Identify the preparation type.
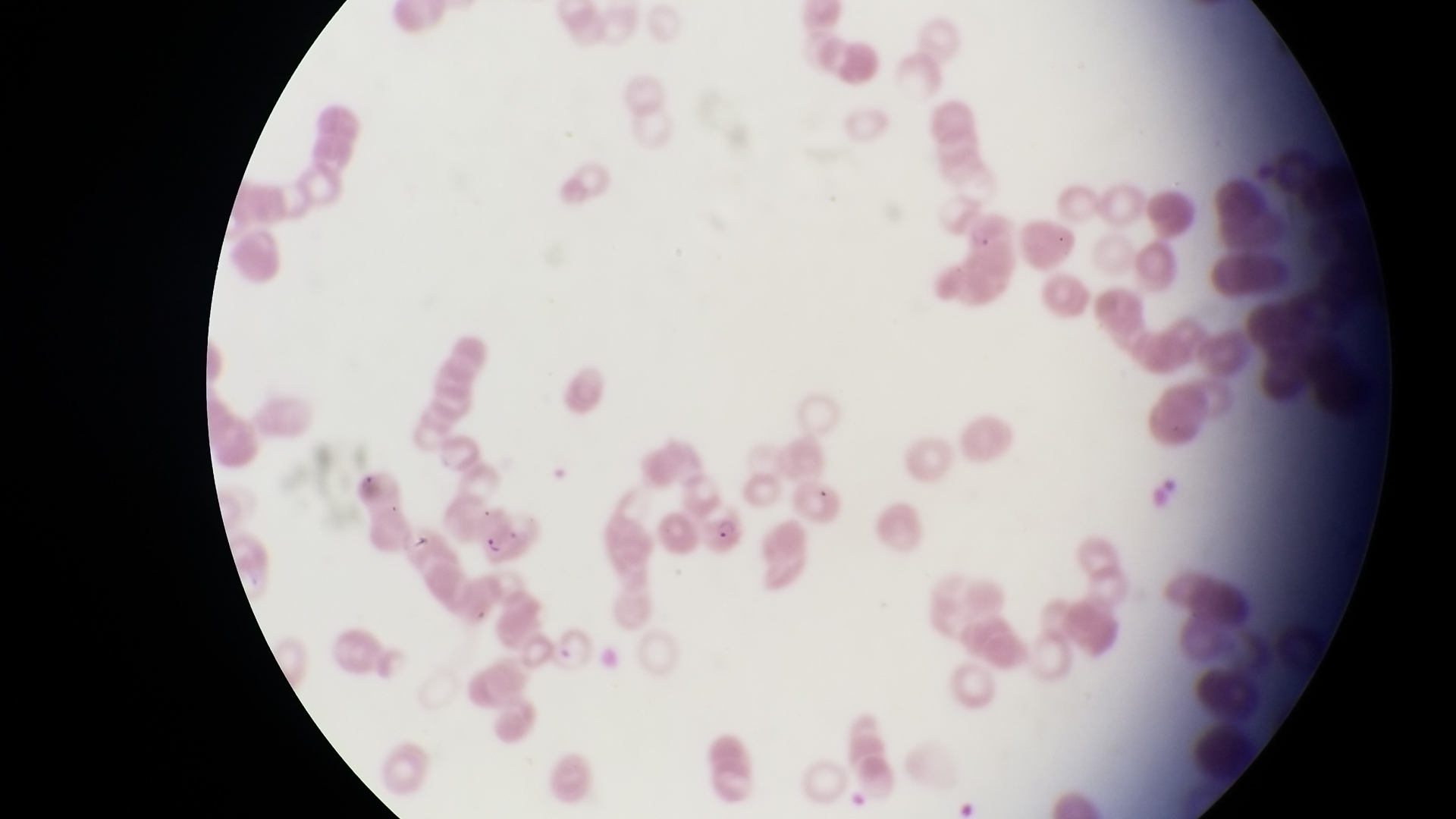

Thin blood film.

{
  "parasitised_red_blood_cell_locations": "approximate bounding boxes as left top right bottom in pixels: 697 504 743 562",
  "field_of_view": "single",
  "country": "Uganda",
  "capture": "smartphone photograph through the eyepiece of an Olympus CX-23 microscope",
  "image_size": "1456×819 pixels",
  "magnification": "1000x"
}